Locate every Plasmodium ovale-infected red blood cell.
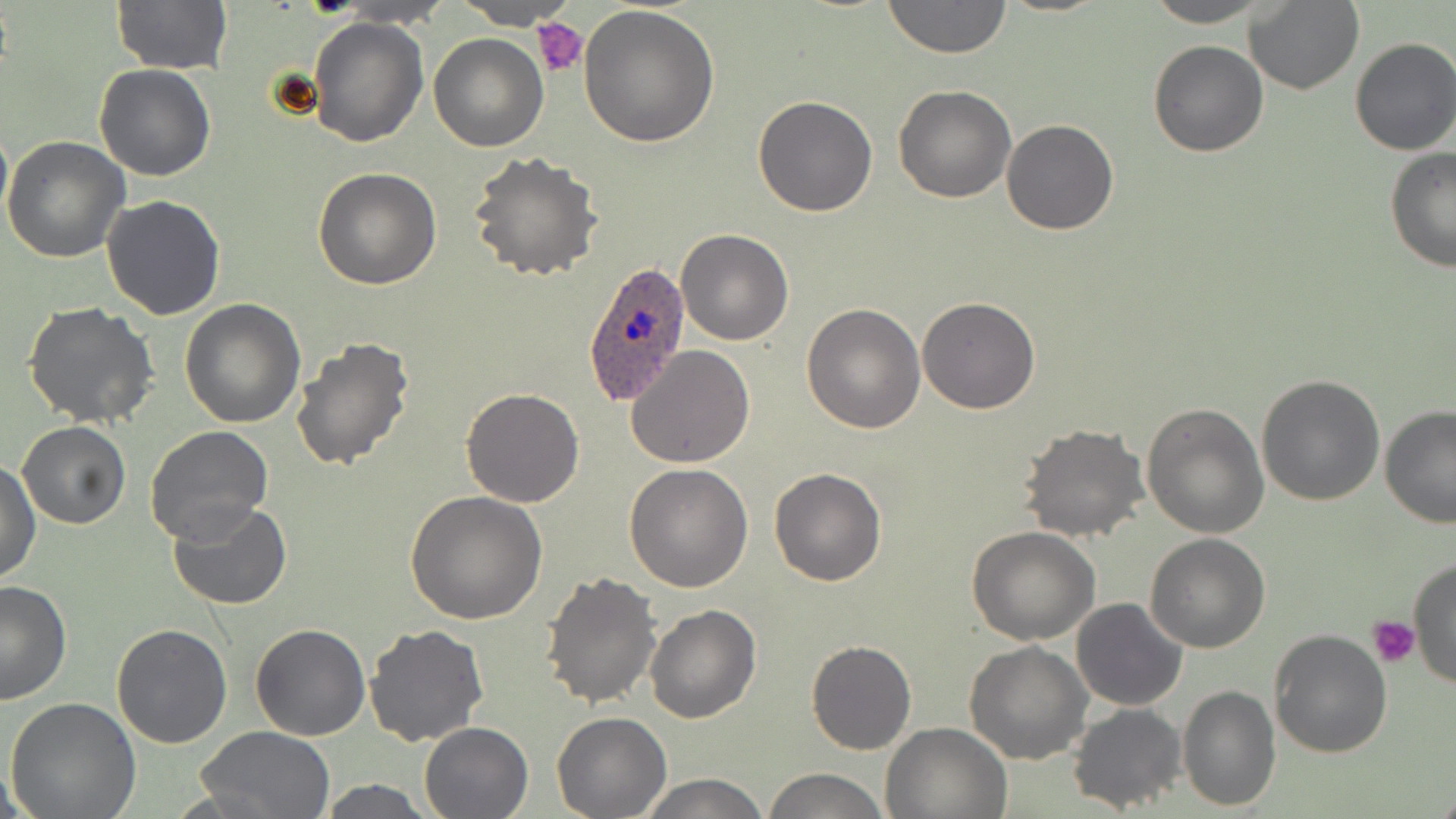

Approximate bounding boxes as (x1, y1, x2, y2) in pixels.
Plasmodium ovale-infected red blood cells: (581, 262, 694, 406).

slide-level diagnosis = Plasmodium ovale
image size = 1456×819 pixels
platelet locations = approximate bounding boxes as (x1, y1, x2, y2) in pixels: (531, 18, 588, 79), (1370, 616, 1420, 668)
magnification = 1000x
field of view = one of a larger specimen
modality = light microscopy
uninfected red blood cell locations = approximate bounding boxes as (x1, y1, x2, y2) in pixels: (109, 0, 232, 76), (455, 0, 579, 29), (881, 0, 1013, 57), (1142, 0, 1277, 27), (1244, 1, 1364, 95), (577, 4, 720, 147), (307, 18, 428, 147), (428, 33, 547, 150), (1349, 36, 1456, 156), (1148, 39, 1268, 157), (95, 65, 216, 182), (893, 85, 1015, 203), (752, 95, 879, 217), (0, 115, 12, 233), (1001, 120, 1118, 235), (2, 135, 131, 262), (1383, 146, 1456, 273), (468, 151, 602, 282), (313, 167, 441, 290), (101, 194, 227, 320), (675, 229, 793, 346), (916, 296, 1040, 413), (179, 298, 307, 428), (23, 300, 162, 428), (802, 302, 926, 433), (290, 336, 417, 472), (624, 344, 755, 467), (1256, 373, 1386, 506), (460, 388, 585, 508), (1142, 401, 1269, 539), (1379, 406, 1456, 528), (17, 421, 130, 528), (1017, 423, 1149, 542), (145, 426, 273, 544), (1, 461, 41, 584), (623, 463, 753, 592), (769, 467, 886, 587), (403, 490, 549, 626), (167, 500, 293, 610), (967, 527, 1099, 645), (1145, 533, 1271, 653), (1409, 557, 1456, 693), (540, 569, 662, 709), (0, 580, 73, 705), (1072, 598, 1188, 711), (644, 604, 761, 724), (250, 623, 370, 742), (112, 625, 234, 748), (365, 625, 490, 748), (1269, 628, 1395, 758), (805, 639, 916, 755), (964, 640, 1093, 765), (1177, 685, 1280, 810), (4, 697, 142, 819), (1067, 703, 1186, 815), (551, 712, 671, 818), (420, 721, 533, 818), (880, 722, 1010, 818), (193, 726, 338, 818), (761, 768, 891, 819), (635, 773, 772, 818), (316, 779, 438, 817)
stain = May-Grünwald-Giemsa
preparation = thin blood film